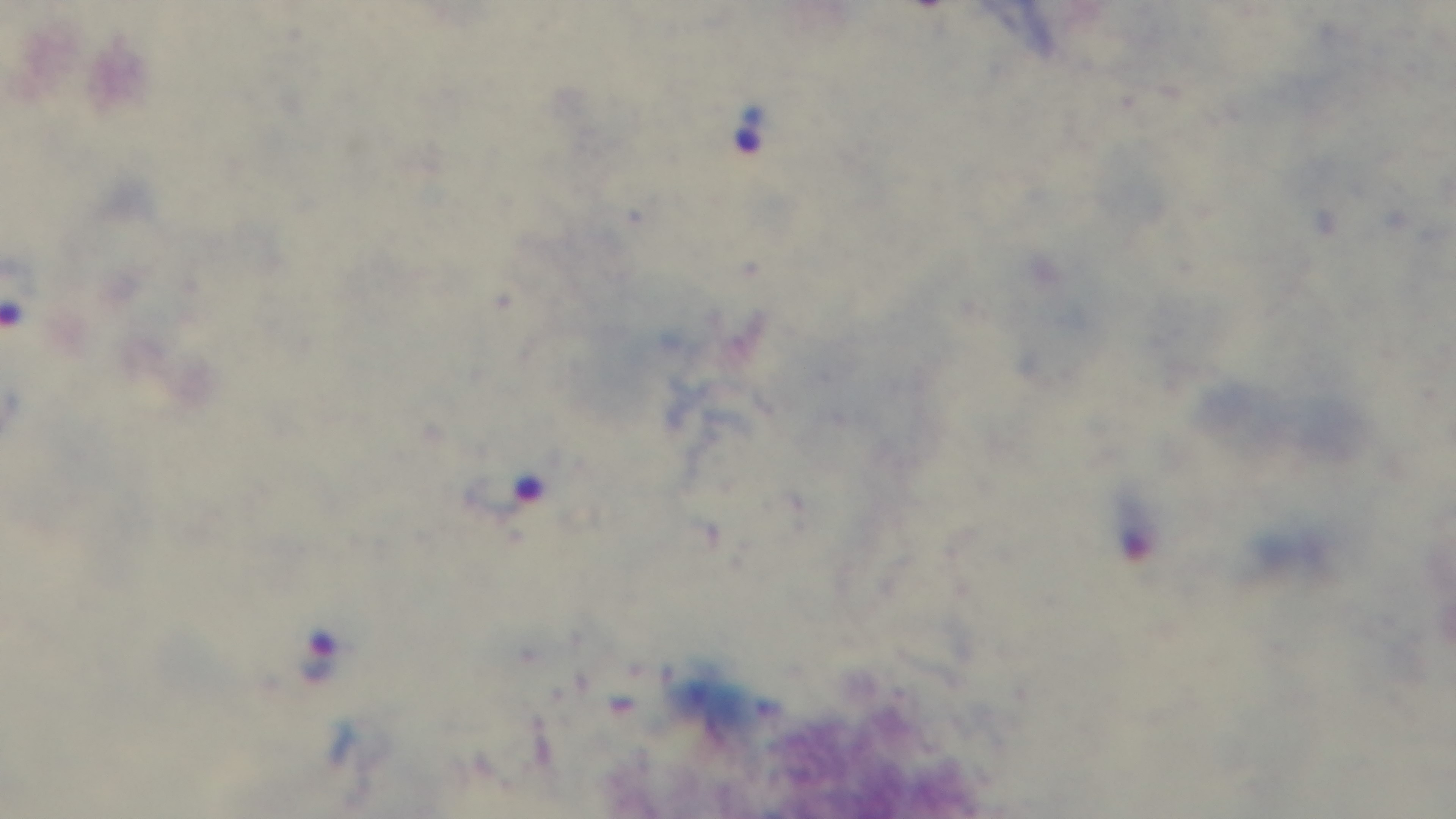

capture = mounted 4K digital camera
field of view = single
objective = 100x oil immersion
modality = light microscopy
malaria status = positive
stain = Giemsa
preparation = thick